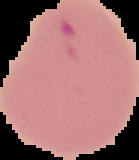 Image is 139×160 pixels. The area outside the segmented cell region is set to black. From a thin blood smear. Result: malaria parasites identified.